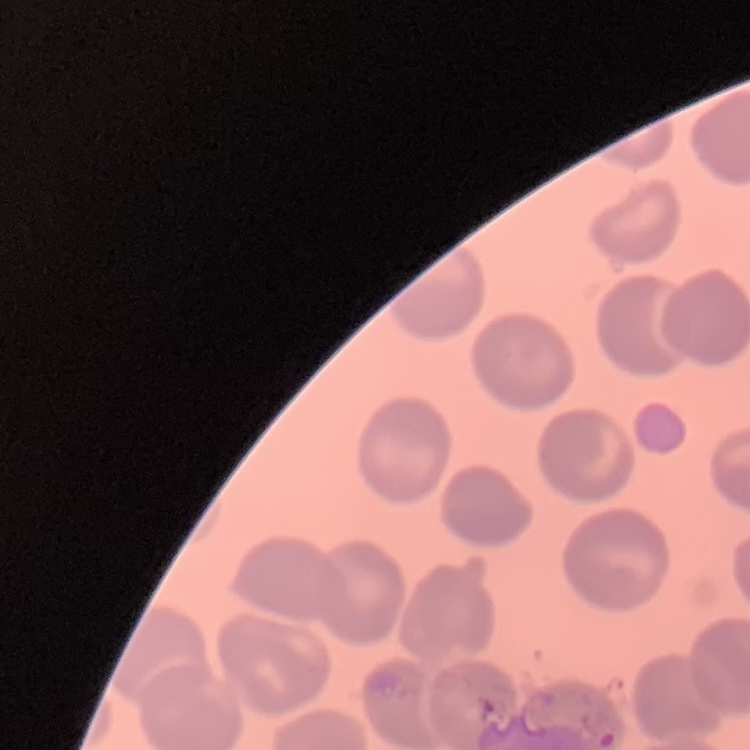
Summary:
  - Erythrocyte morphology: no rouleaux formation
  - Stain: Field's or Giemsa
  - Image type: one tile cut from a larger photomicrograph
  - Preparation: thin blood smear